Assess the morphology of the red blood cells.
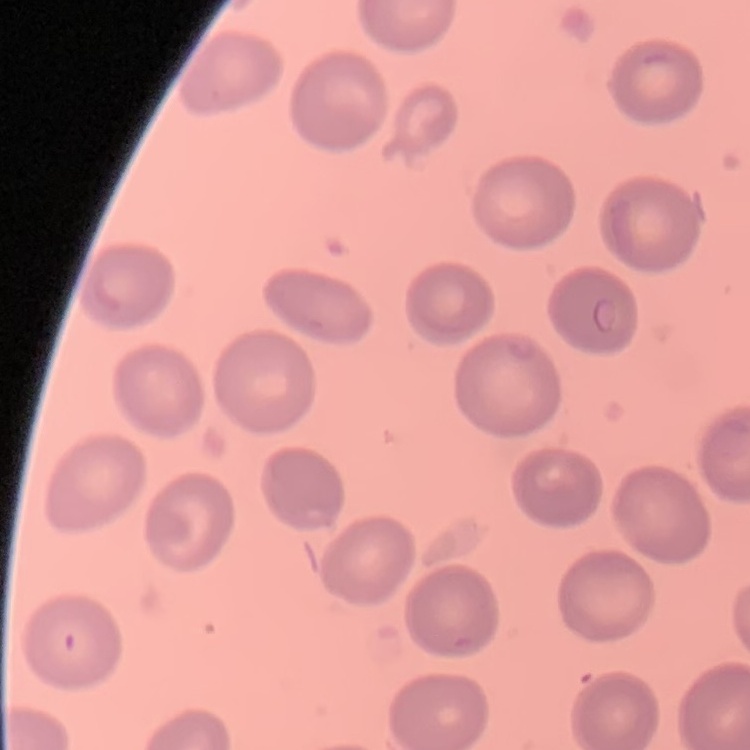

They show no rouleaux formation.

Summary:
  - Preparation: thin blood smear
  - Image type: square crop of a larger photomicrograph
  - Stain: Field's or Giemsa